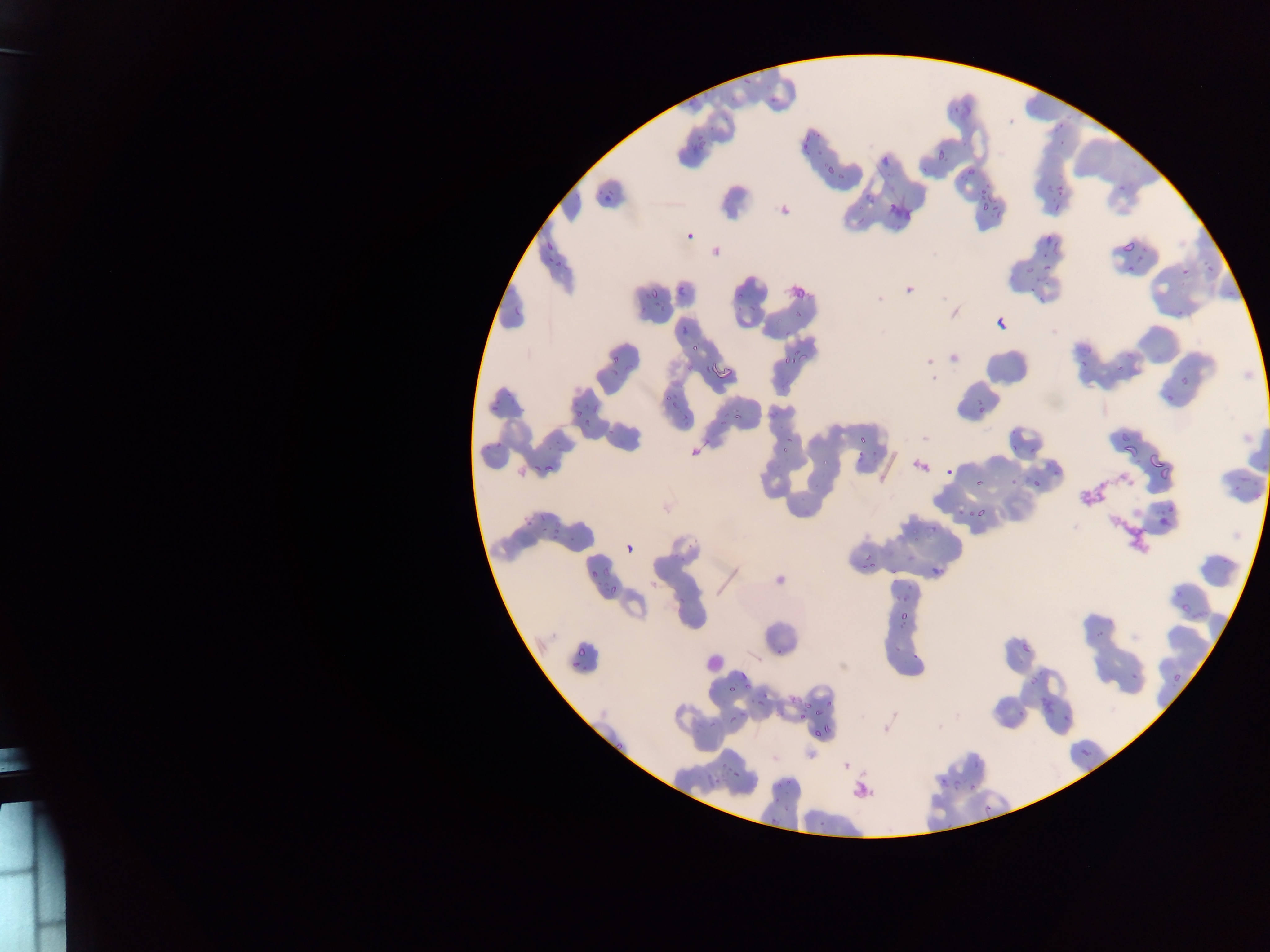
Approximate bounding boxes as [left, top, right, bottom] in pixels.
Summary:
  - Artifact (stain precipitate or debris) locations: [1110, 468, 1140, 497], [1080, 469, 1108, 511], [1104, 513, 1154, 558]
  - Leukocyte locations: [697, 643, 722, 672]
  - Malaria parasite locations: [742, 72, 755, 86], [767, 95, 778, 103], [949, 104, 961, 114], [799, 129, 809, 143], [695, 136, 705, 142], [1057, 136, 1067, 145], [799, 138, 806, 151], [935, 148, 945, 161], [964, 168, 975, 180], [1120, 181, 1129, 194], [981, 182, 988, 195], [1055, 184, 1063, 195], [603, 190, 616, 201], [981, 201, 994, 215], [1051, 204, 1059, 215], [1045, 233, 1050, 244], [1120, 235, 1134, 254], [1052, 238, 1061, 254], [545, 240, 556, 250], [1136, 244, 1147, 251], [545, 254, 552, 263], [555, 256, 563, 267], [1134, 257, 1146, 263], [1038, 263, 1053, 274], [1179, 264, 1192, 276], [1023, 265, 1037, 273], [1126, 265, 1132, 275], [1206, 265, 1215, 272], [1031, 273, 1045, 285], [675, 286, 688, 296], [649, 287, 660, 299], [1038, 289, 1049, 303], [735, 293, 744, 304], [750, 300, 761, 313], [513, 306, 525, 316], [1177, 306, 1185, 314], [654, 307, 664, 314], [795, 310, 804, 318], [679, 325, 690, 337], [780, 329, 795, 342], [691, 344, 700, 350], [778, 348, 803, 374], [611, 351, 621, 363], [1081, 361, 1089, 367], [1113, 361, 1125, 371], [704, 364, 709, 372], [609, 371, 620, 377], [1180, 377, 1188, 386], [1164, 392, 1176, 403], [664, 394, 673, 403], [489, 399, 501, 413], [974, 406, 988, 420], [572, 409, 583, 420], [733, 412, 746, 421], [681, 415, 689, 423], [719, 418, 727, 429], [584, 422, 592, 429], [609, 427, 616, 435], [778, 434, 796, 456], [857, 434, 871, 444], [497, 435, 507, 446], [1121, 438, 1137, 457], [1012, 441, 1019, 451], [484, 444, 492, 451], [1030, 445, 1037, 454], [858, 449, 863, 458], [871, 450, 880, 457], [1149, 456, 1171, 479], [822, 458, 830, 466], [532, 460, 544, 472], [543, 465, 556, 471], [945, 466, 955, 477], [1008, 475, 1017, 485], [973, 477, 987, 487], [1031, 478, 1045, 492], [1233, 479, 1242, 494], [965, 504, 987, 523], [1164, 504, 1174, 512], [957, 508, 965, 515], [532, 515, 550, 525], [1160, 518, 1170, 526], [554, 522, 565, 530], [549, 529, 562, 539], [624, 535, 641, 557], [912, 536, 918, 544], [929, 553, 948, 576], [861, 558, 880, 575], [588, 566, 600, 579], [605, 566, 612, 575], [891, 569, 899, 575], [609, 584, 617, 595], [895, 592, 903, 601], [678, 597, 690, 604], [1181, 605, 1191, 614], [900, 607, 911, 621], [1094, 630, 1104, 639], [1021, 641, 1032, 655], [777, 643, 786, 651], [577, 644, 591, 660], [911, 648, 921, 659], [736, 669, 751, 686], [1130, 672, 1134, 681], [1172, 675, 1184, 688], [730, 682, 738, 693], [760, 693, 770, 701], [753, 699, 767, 709], [825, 700, 834, 707], [814, 707, 825, 718], [1061, 707, 1073, 722], [799, 710, 808, 720], [1018, 711, 1024, 721], [823, 717, 836, 732], [728, 718, 737, 725], [707, 721, 719, 732], [812, 727, 826, 737], [611, 738, 626, 751], [1078, 744, 1095, 764], [973, 760, 983, 769], [717, 765, 727, 772], [733, 767, 743, 776], [938, 773, 949, 786], [714, 777, 722, 788], [784, 778, 790, 786], [952, 781, 960, 792], [967, 785, 972, 793], [781, 800, 793, 809], [765, 812, 770, 823] | approximate [x, y] pixel centers of objects too small to bound: [1060, 124], [1032, 289], [1257, 495], [899, 647], [574, 663], [810, 705], [742, 716], [778, 784], [776, 798]
  - Field of view: single
  - Image size: 1270×952 pixels
  - Preparation: thin blood smear
  - Country: Ghana
  - Capture: mobile-phone photograph through a microscope